Comment on the morphology of the red blood cells.
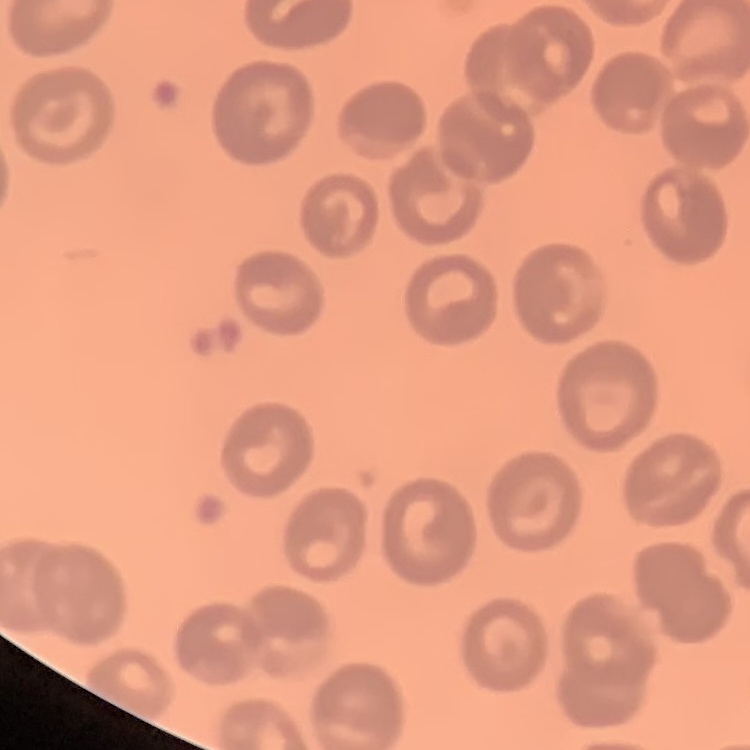

No rouleaux formation.

{
  "image_type": "square crop of a larger photomicrograph",
  "preparation": "thin blood smear",
  "stain": "Field's or Giemsa"
}